Classify this cell by malaria status.
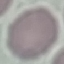

It is uninfected.

{
  "image_type": "cell patch, automatically extracted from a larger field of view and resized to 64 × 64 pixels",
  "stain": "Giemsa",
  "preparation": "thin blood smear",
  "capture": "smartphone camera at the microscope eyepiece"
}